Locate and identify every blood parasite.
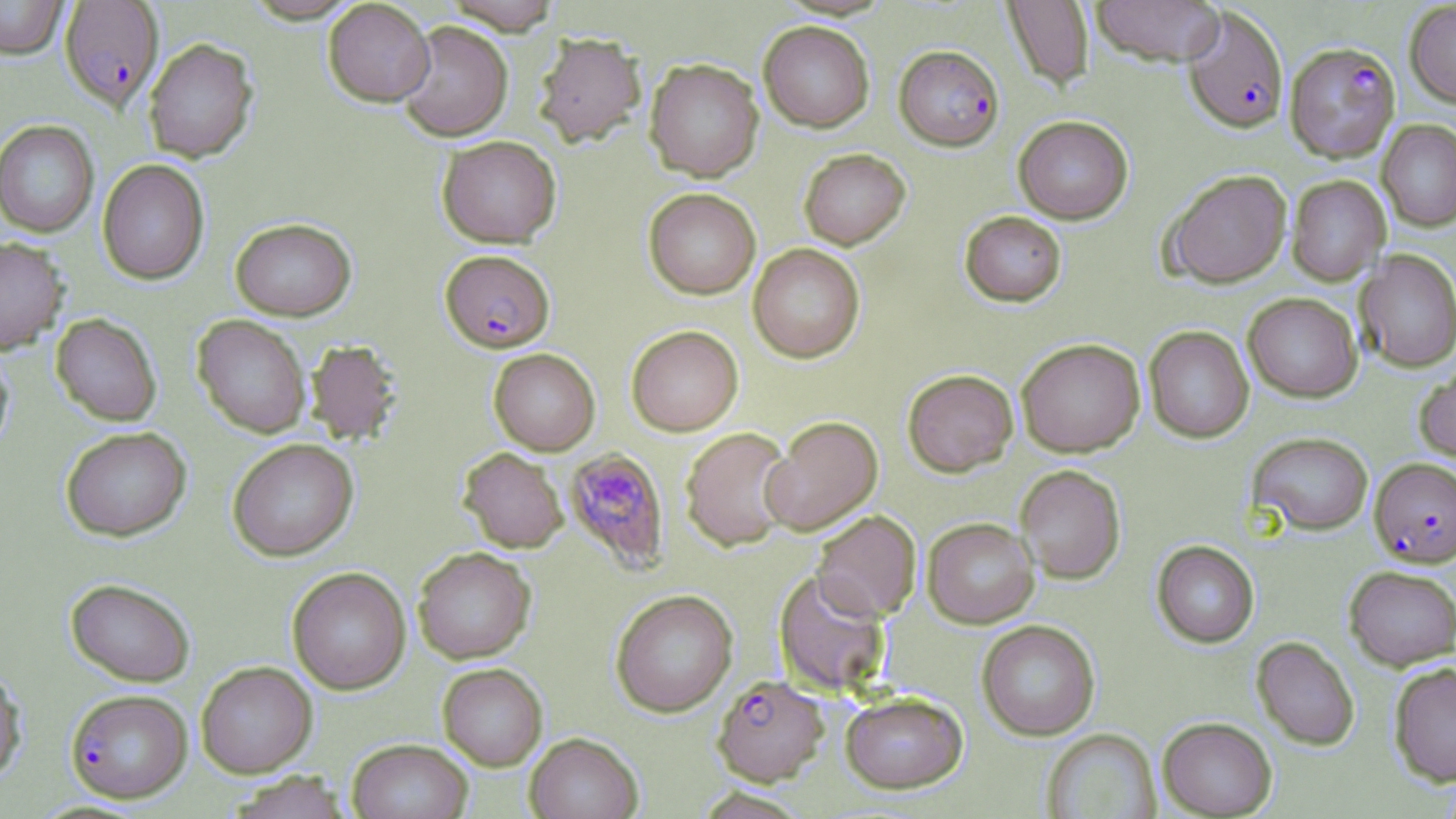

Approximate bounding boxes as [x1, y1, x2, y2] in pixels.
Plasmodium falciparum-infected red blood cells: [59, 0, 164, 112], [1183, 5, 1289, 134], [1285, 41, 1400, 164], [895, 45, 1004, 150], [440, 249, 555, 352], [563, 447, 669, 572], [1370, 457, 1456, 567], [712, 674, 829, 786], [65, 688, 192, 802].
No Plasmodium ovale, Plasmodium malariae, Plasmodium vivax, Babesia divergens, or Trypanosoma brucei observed.

Uninfected red blood cell locations: [0, 0, 69, 59], [242, 0, 363, 23], [443, 0, 564, 34], [1092, 0, 1226, 66], [323, 1, 435, 106], [1002, 1, 1094, 91], [1405, 1, 1456, 107], [759, 20, 874, 132], [396, 21, 513, 141], [534, 31, 647, 148], [143, 38, 258, 163], [644, 58, 764, 182], [1013, 115, 1133, 223], [1377, 119, 1456, 232], [0, 120, 99, 238], [436, 135, 562, 248], [798, 148, 910, 250], [97, 159, 209, 285], [1163, 169, 1292, 288], [1287, 175, 1390, 285], [643, 187, 761, 299], [959, 210, 1067, 307], [230, 217, 356, 320], [0, 236, 69, 355], [748, 243, 865, 363], [1355, 250, 1456, 372], [1243, 292, 1362, 402], [51, 314, 162, 426], [193, 315, 311, 438], [626, 325, 743, 436], [1143, 325, 1254, 443], [1016, 337, 1145, 457], [304, 339, 404, 446], [0, 348, 13, 456], [489, 348, 600, 455], [1415, 361, 1456, 464], [902, 369, 1018, 476], [761, 415, 883, 535], [60, 426, 191, 541], [680, 427, 795, 552], [1248, 431, 1374, 535], [227, 438, 358, 561], [458, 447, 568, 553], [1015, 464, 1126, 584], [811, 510, 921, 621], [922, 517, 1039, 629], [1152, 540, 1259, 648], [413, 547, 536, 663], [1344, 565, 1456, 670], [287, 567, 411, 694], [773, 569, 891, 696], [66, 577, 195, 687], [610, 589, 738, 717], [977, 620, 1100, 741], [1251, 636, 1360, 751], [195, 661, 317, 777], [1388, 662, 1456, 786], [438, 663, 548, 770], [0, 665, 27, 785], [840, 691, 969, 794], [1157, 717, 1277, 818], [1041, 728, 1161, 819], [525, 732, 643, 819], [347, 738, 473, 819], [223, 771, 353, 819]. Slide-level diagnosis: Plasmodium falciparum. Single field of view. May-Grünwald-Giemsa-stained preparation. 1000x magnification. Optical microscopy. Thin blood film. Image is 1456×819 pixels.